Name the cell type shown.
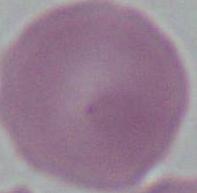
This is an erythrocyte.

modality: photomicrograph
magnification: 1000x